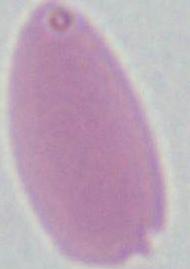
Summary:
  - Modality: photomicrograph
  - Identification: red blood cell
  - Magnification: 1000x